Point out every Plasmodium parasite.
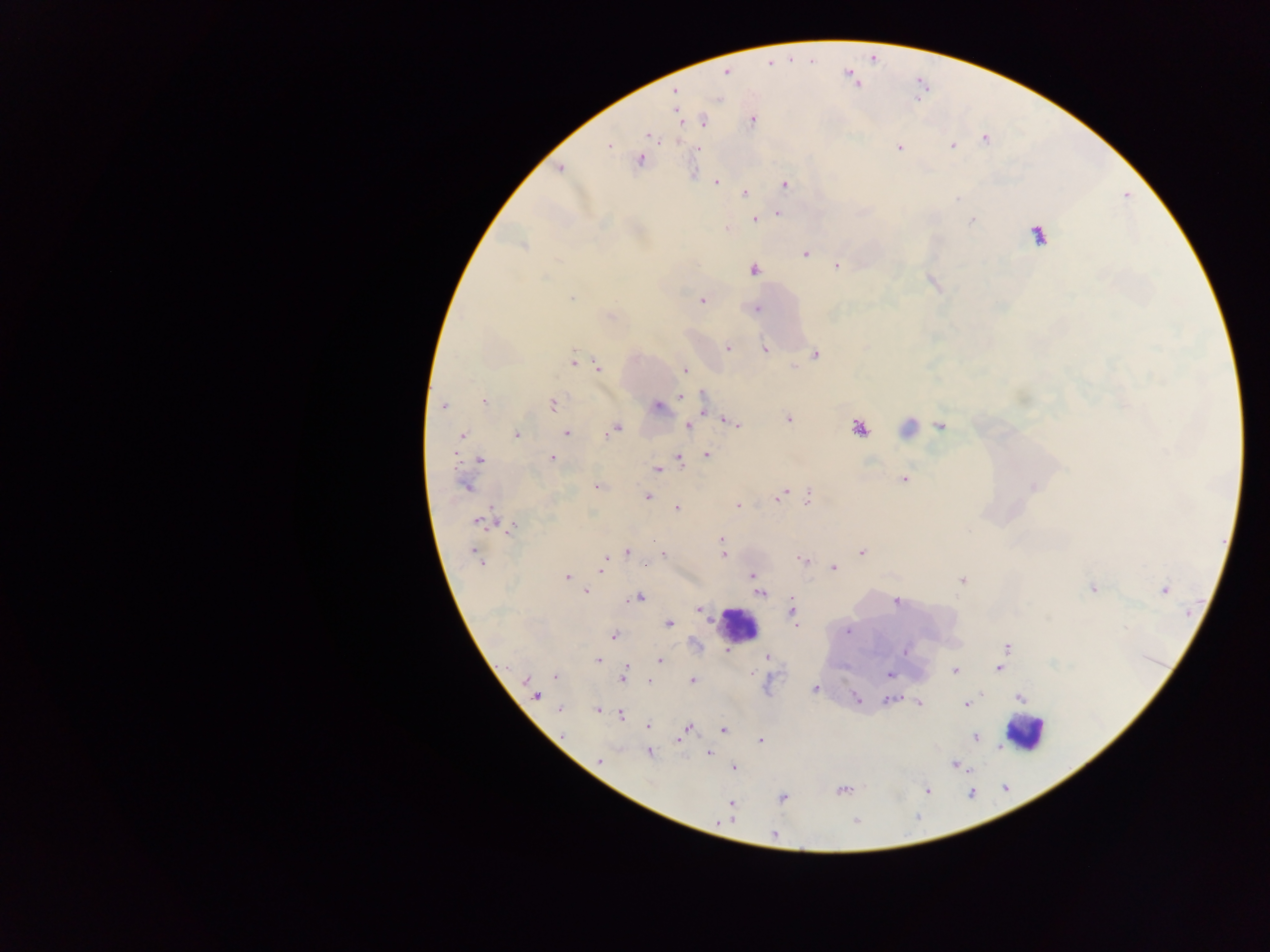

Approximate centers as [x, y] in pixels.
Plasmodium parasites: [769, 63], [727, 70], [675, 92], [704, 120], [752, 120], [649, 135], [985, 139], [609, 145], [953, 146], [899, 148], [699, 149], [639, 161], [560, 167], [715, 182], [785, 184], [745, 193], [957, 198], [778, 213], [755, 220], [971, 221], [726, 228], [1038, 236], [524, 246], [805, 254], [837, 266], [754, 270], [571, 299], [702, 300], [757, 308], [728, 348], [765, 350], [815, 353], [573, 359], [598, 368], [685, 370], [702, 396], [680, 397], [484, 401], [553, 404], [443, 406], [657, 407], [789, 419], [730, 422], [940, 425], [688, 426], [860, 428], [615, 429], [566, 432], [516, 434], [462, 436], [454, 453], [707, 455], [552, 458], [480, 460], [680, 460], [657, 469], [905, 478], [465, 486], [597, 486], [1033, 487], [782, 494], [648, 496], [778, 498], [808, 498], [738, 506], [677, 508], [477, 521], [511, 528], [721, 540], [722, 548], [628, 552], [861, 552], [663, 554], [723, 554], [476, 555], [479, 560], [803, 560], [603, 564], [833, 568], [601, 570], [752, 575], [566, 576], [962, 579], [1093, 589], [1164, 590], [585, 591], [760, 593], [638, 598], [895, 602], [699, 609], [792, 611], [669, 623], [847, 632], [614, 636], [1007, 647], [905, 651], [768, 657], [598, 659], [660, 660], [999, 668], [625, 669], [955, 670], [889, 675], [555, 676], [623, 676], [693, 680], [649, 682], [814, 689], [536, 696], [856, 698], [1020, 698], [888, 700], [919, 703], [966, 705], [559, 710], [597, 710], [621, 715], [648, 726], [687, 729], [724, 730], [684, 733], [976, 736], [678, 740], [761, 741], [649, 753], [710, 753], [600, 761], [956, 764], [733, 767], [841, 790], [927, 791], [782, 798], [731, 803], [855, 822], [773, 834].

{
  "country": "Ghana",
  "preparation": "thick blood film",
  "leukocyte_locations": "approximate centers as [x, y] in pixels: [738, 625], [1024, 732]",
  "image_size": "1270×952 pixels",
  "field_of_view": "single",
  "capture": "mobile-phone photograph through a microscope"
}